Outline each blood parasite and name the species.
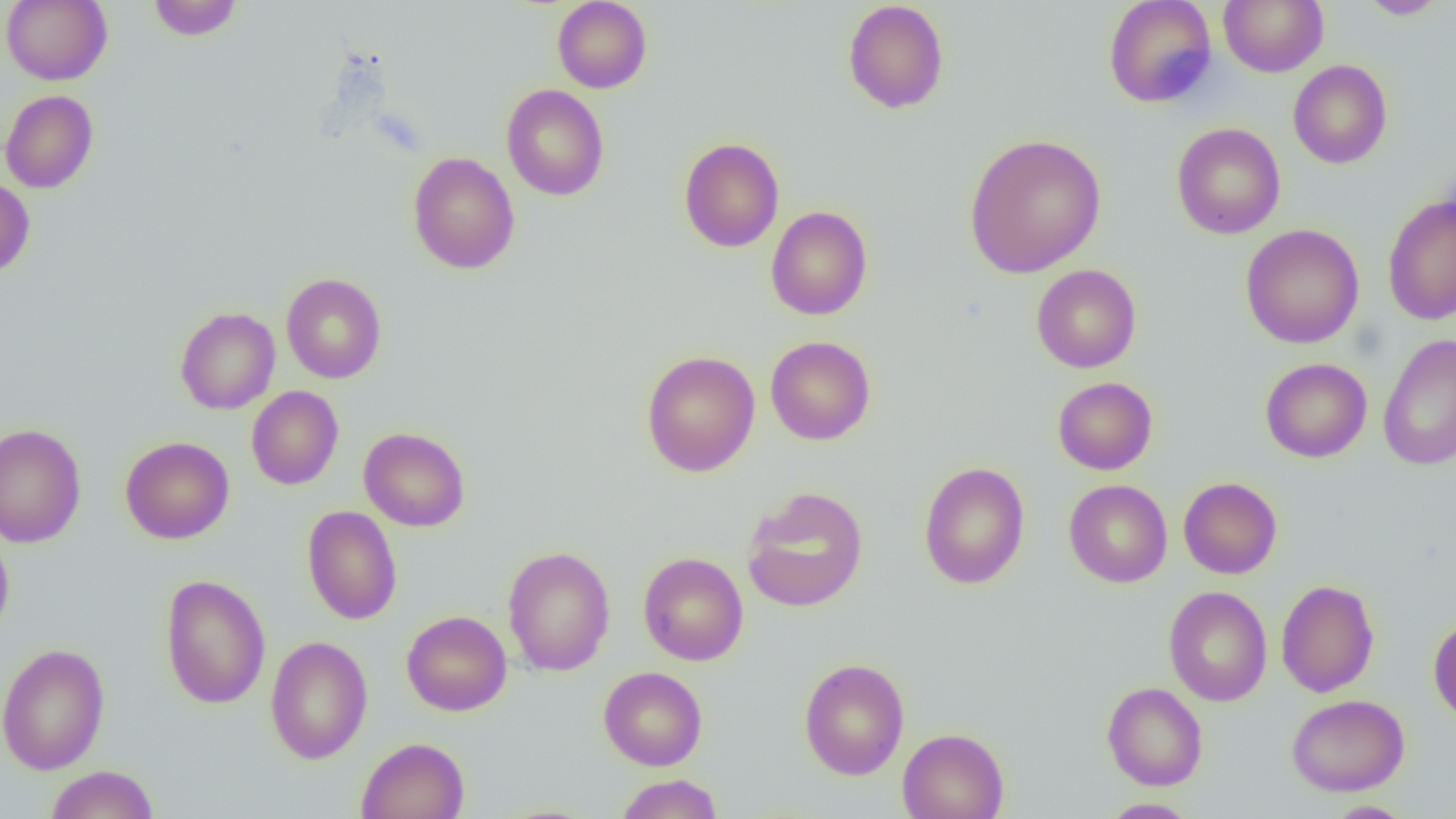

No blood parasites observed.

Summary:
  - Coordinate format: approximate bounding boxes as named x1/y1/x2/y2 corners in pixels
  - Uninfected red blood cell locations: (x1=1, y1=0, x2=112, y2=85), (x1=147, y1=0, x2=243, y2=41), (x1=552, y1=0, x2=652, y2=93), (x1=842, y1=0, x2=949, y2=114), (x1=1102, y1=0, x2=1218, y2=108), (x1=1218, y1=0, x2=1328, y2=76), (x1=1358, y1=1, x2=1449, y2=19), (x1=1288, y1=60, x2=1393, y2=169), (x1=501, y1=84, x2=610, y2=201), (x1=0, y1=89, x2=99, y2=193), (x1=1171, y1=122, x2=1285, y2=240), (x1=963, y1=133, x2=1107, y2=279), (x1=678, y1=137, x2=784, y2=252), (x1=407, y1=152, x2=521, y2=274), (x1=0, y1=177, x2=35, y2=277), (x1=1383, y1=196, x2=1456, y2=325), (x1=766, y1=206, x2=873, y2=320), (x1=1240, y1=223, x2=1364, y2=348), (x1=1031, y1=264, x2=1141, y2=373), (x1=281, y1=273, x2=387, y2=383), (x1=175, y1=306, x2=281, y2=415), (x1=1378, y1=334, x2=1456, y2=471), (x1=765, y1=336, x2=876, y2=445), (x1=641, y1=350, x2=760, y2=477), (x1=1260, y1=358, x2=1372, y2=463), (x1=1052, y1=377, x2=1158, y2=475), (x1=246, y1=386, x2=344, y2=490), (x1=0, y1=423, x2=86, y2=548), (x1=358, y1=427, x2=471, y2=531), (x1=120, y1=436, x2=234, y2=544), (x1=918, y1=461, x2=1030, y2=589), (x1=1179, y1=477, x2=1282, y2=579), (x1=1063, y1=479, x2=1173, y2=587), (x1=741, y1=486, x2=869, y2=613), (x1=302, y1=505, x2=402, y2=625), (x1=0, y1=529, x2=14, y2=641), (x1=502, y1=545, x2=616, y2=676), (x1=638, y1=552, x2=749, y2=665), (x1=159, y1=574, x2=271, y2=709), (x1=1276, y1=579, x2=1379, y2=697), (x1=1164, y1=586, x2=1272, y2=706), (x1=401, y1=610, x2=512, y2=715), (x1=1428, y1=616, x2=1456, y2=725), (x1=265, y1=635, x2=373, y2=764), (x1=0, y1=643, x2=111, y2=774), (x1=798, y1=658, x2=910, y2=780), (x1=598, y1=666, x2=708, y2=770), (x1=1102, y1=682, x2=1208, y2=791), (x1=1286, y1=693, x2=1410, y2=796), (x1=897, y1=728, x2=1010, y2=819), (x1=356, y1=737, x2=469, y2=819), (x1=45, y1=765, x2=160, y2=819), (x1=614, y1=774, x2=725, y2=818), (x1=1098, y1=799, x2=1200, y2=818), (x1=1323, y1=800, x2=1417, y2=819)
  - Slide-level diagnosis: negative for blood parasites
  - Field of view: single
  - Modality: optical microscopy
  - Magnification: 1000x
  - Preparation: thin blood smear
  - Image size: 1456×819 pixels